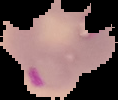

Summary:
  - Result: Plasmodium parasites detected
  - Image size: 118×100 pixels
  - Image type: segmented cell region with the area outside set to black
  - Preparation: thin blood film